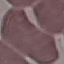
result = no malaria parasites detected
preparation = thin smear
image type = automatically extracted cell patch, resized to 64 × 64 pixels
stain = Giemsa
capture = smartphone camera at the microscope eyepiece